Describe the morphology of the red blood cells.
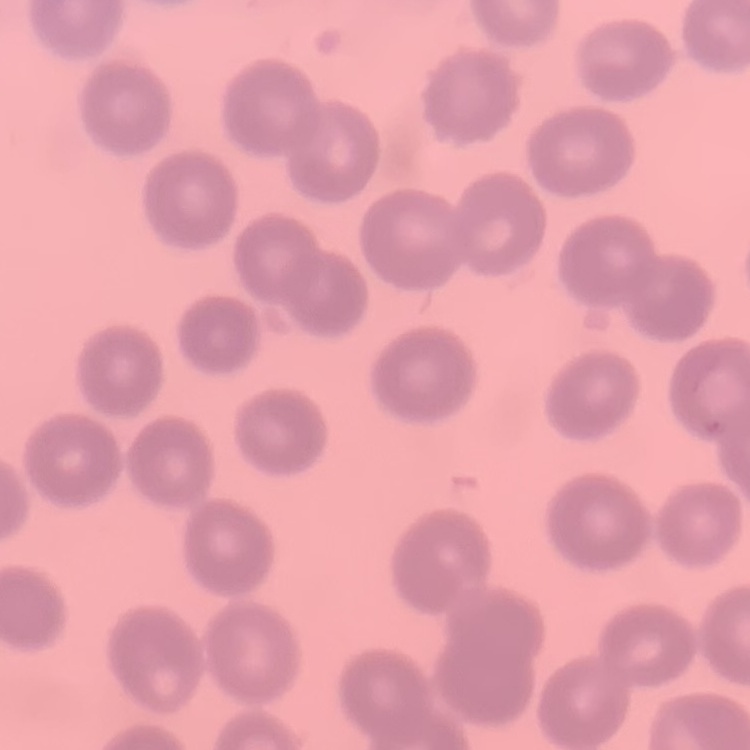

They show no rouleaux formation.

{
  "image_type": "one tile cut from a larger photomicrograph",
  "stain": "Field's or Giemsa",
  "preparation": "thin blood smear"
}